Assess this cell for malaria.
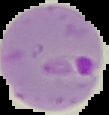
Parasitized.

{
  "image_size": "109×115 pixels",
  "preparation": "thin blood film",
  "image_type": "cell region segmented out of the field of view; surrounding area masked to black"
}